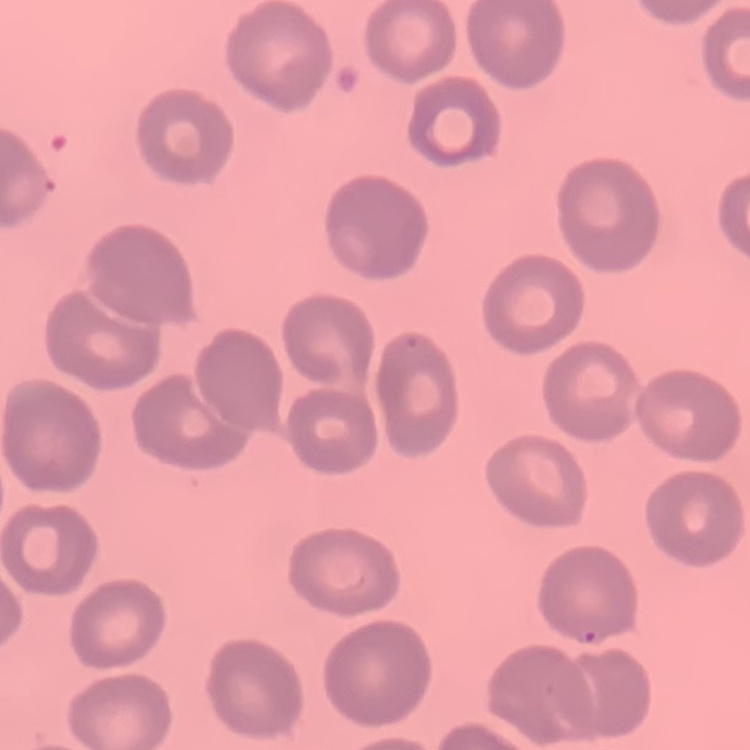 The erythrocytes show no rouleaux formation. One tile cut from a larger photomicrograph. Thin blood smear. Field's or Giemsa stain.